Assess this cell for malaria.
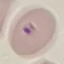

It is parasitized.

Giemsa stain. Thin blood smear. Cell patch, automatically extracted from a larger field of view and resized to 64 × 64 pixels. Photographed with a smartphone camera at the microscope eyepiece.